Classify this cell by malaria status.
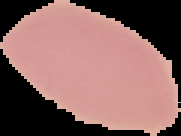
Uninfected.

image type = cell region segmented out of the field of view; surrounding area masked to black
preparation = thin blood film
image size = 181×136 pixels